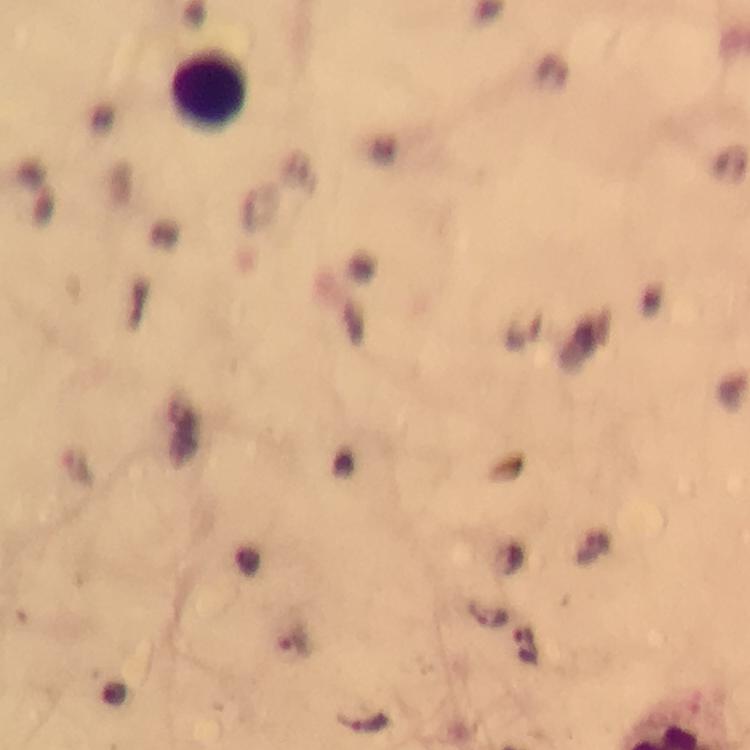
Approximate centers as (x, y) in pixels.
Summary:
  - Plasmodium parasite locations: (489, 617), (293, 643), (526, 647), (365, 724)
  - Leukocyte locations: (209, 93)
  - Preparation: thick blood smear
  - Immersion oil: used
  - Stain: Giemsa
  - Capture: smartphone camera through the microscope
  - Magnification: 100x
  - Cropped from: a single field of view
  - Image size: 750×750 pixels
  - Context: from a malaria diagnostic workup